Classify this cell by malaria status.
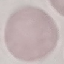
It is uninfected.

Summary:
  - Preparation: thin blood film
  - Stain: Giemsa
  - Image type: automatically extracted cell patch, resized to 64 × 64 pixels
  - Capture: smartphone camera at the microscope eyepiece